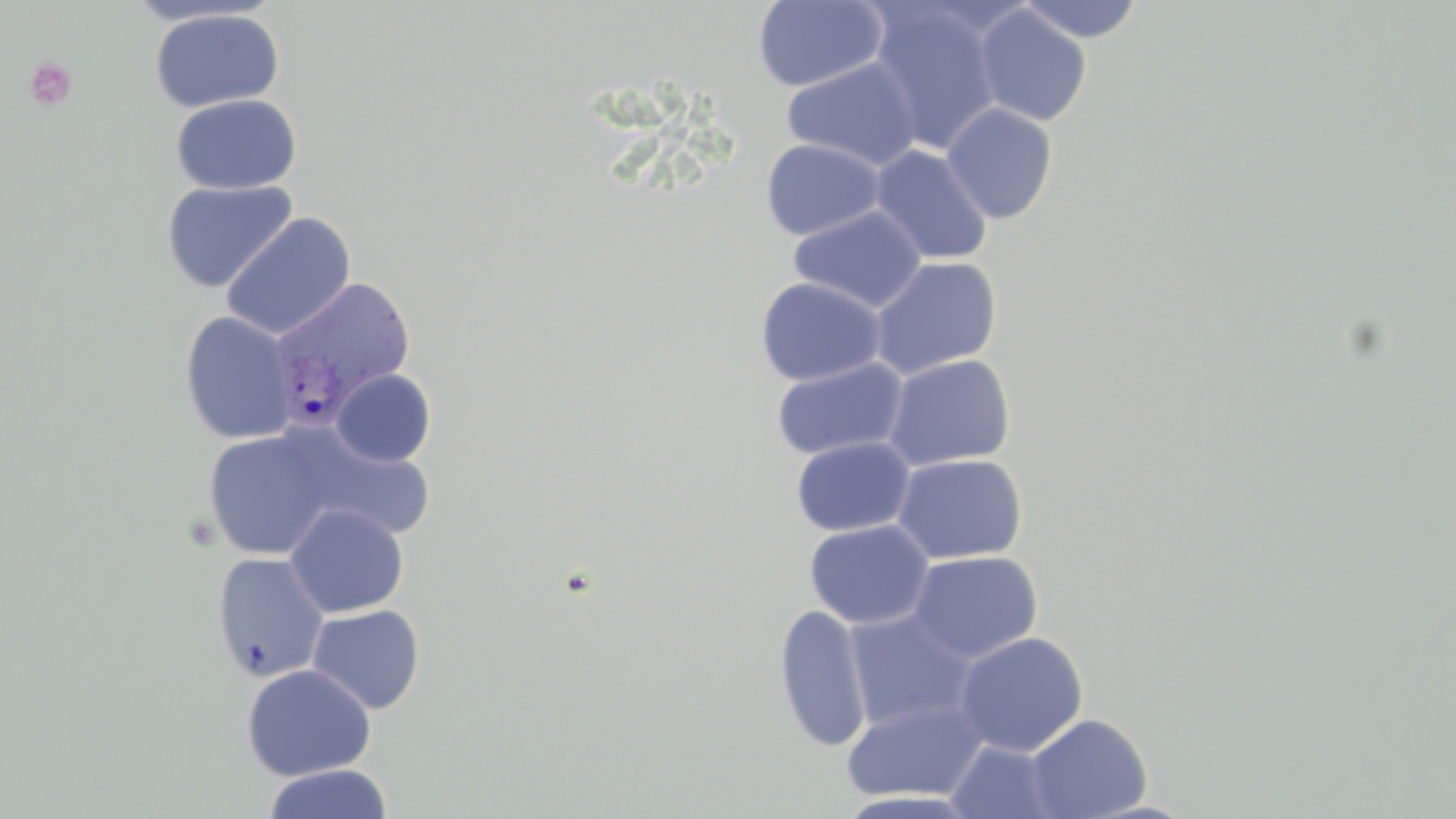

Summary:
  - Coordinate format: approximate bounding boxes as (x1, y1, x2, y2) in pixels
  - Plasmodium vivax-infected red blood cell locations: (268, 274, 418, 427)
  - Uninfected red blood cell locations: (753, 0, 889, 92), (1017, 0, 1145, 43), (866, 1, 1004, 154), (973, 5, 1092, 126), (149, 8, 284, 113), (782, 57, 922, 171), (170, 93, 302, 195), (941, 103, 1058, 224), (760, 138, 884, 241), (870, 144, 993, 265), (160, 179, 298, 293), (789, 205, 926, 312), (220, 212, 356, 341), (869, 256, 1003, 379), (755, 277, 886, 386), (180, 311, 297, 445), (883, 353, 1015, 470), (770, 357, 909, 461), (331, 369, 436, 467), (283, 425, 436, 543), (203, 429, 337, 560), (791, 436, 914, 536), (892, 453, 1028, 564), (284, 503, 408, 618), (804, 519, 934, 628), (907, 550, 1043, 663), (212, 552, 329, 682), (307, 604, 425, 714), (773, 604, 873, 753), (842, 608, 979, 733), (953, 631, 1088, 756), (240, 663, 376, 780), (841, 697, 990, 802), (1026, 713, 1153, 819), (945, 739, 1067, 819), (263, 764, 393, 819)
  - Platelet locations: (24, 56, 77, 112)
  - Slide-level diagnosis: Plasmodium vivax
  - Magnification: 1000x
  - Image size: 1456×819 pixels
  - Stain: May-Grünwald-Giemsa
  - Field of view: one of a larger specimen
  - Modality: optical microscopy
  - Preparation: thin blood film